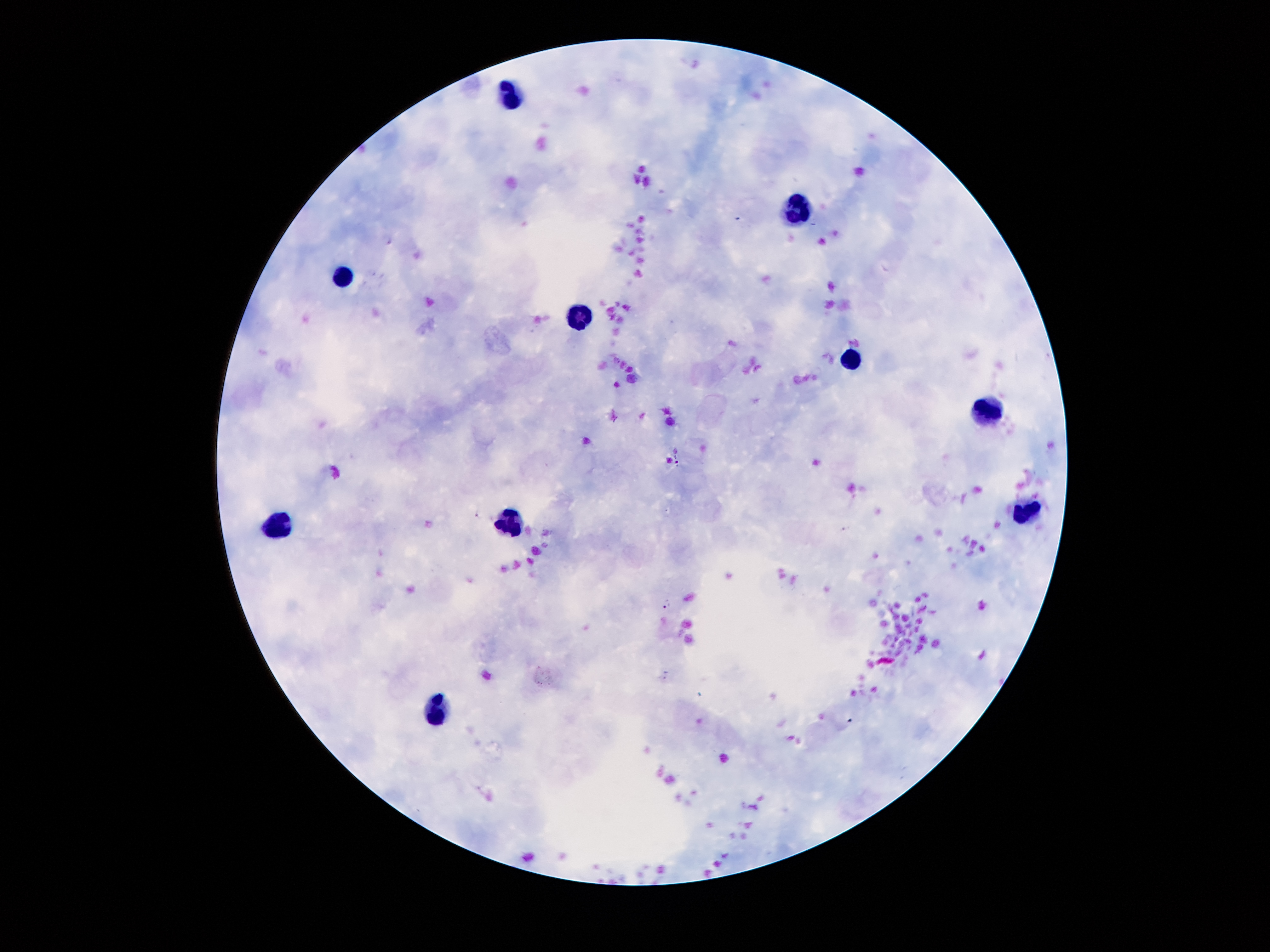
Approximate object centers, in pixels from the top-left corner.
Summary:
  - Leukocyte locations: (x=515, y=101), (x=797, y=212), (x=339, y=275), (x=577, y=315), (x=855, y=364), (x=986, y=413), (x=1025, y=509), (x=511, y=522), (x=279, y=525), (x=436, y=714)
  - Plasmodium parasite locations: (x=388, y=240), (x=678, y=460), (x=479, y=514), (x=667, y=605)
  - Preparation: thick blood film
  - Magnification: 100x
  - Stain: Giemsa
  - Field of view: single
  - Image size: 1270×952 pixels
  - Patient malaria status: positive for Plasmodium falciparum
  - Capture: smartphone camera through the microscope eyepiece